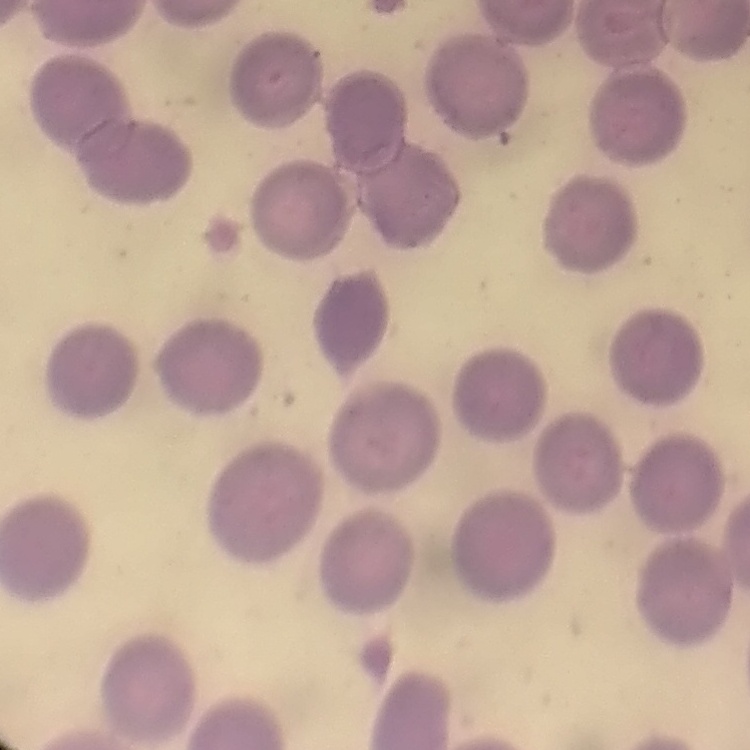
Summary:
  - Erythrocyte morphology: no rouleaux formation
  - Stain: Field's or Giemsa
  - Preparation: thin peripheral smear
  - Image type: square crop of a larger photomicrograph